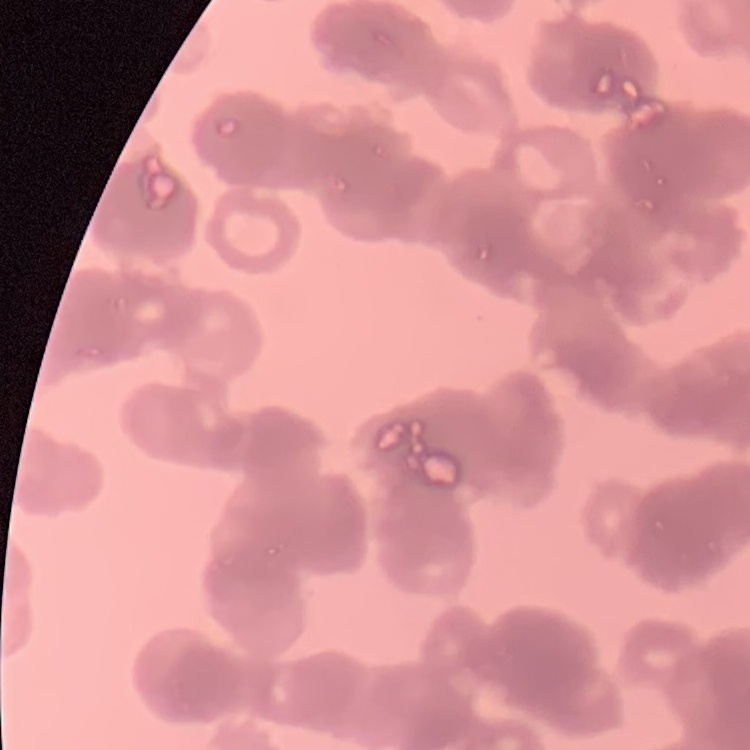 The erythrocytes show rouleaux formation. Square crop of a larger photomicrograph. Field's or Giemsa stain. Thin blood film.